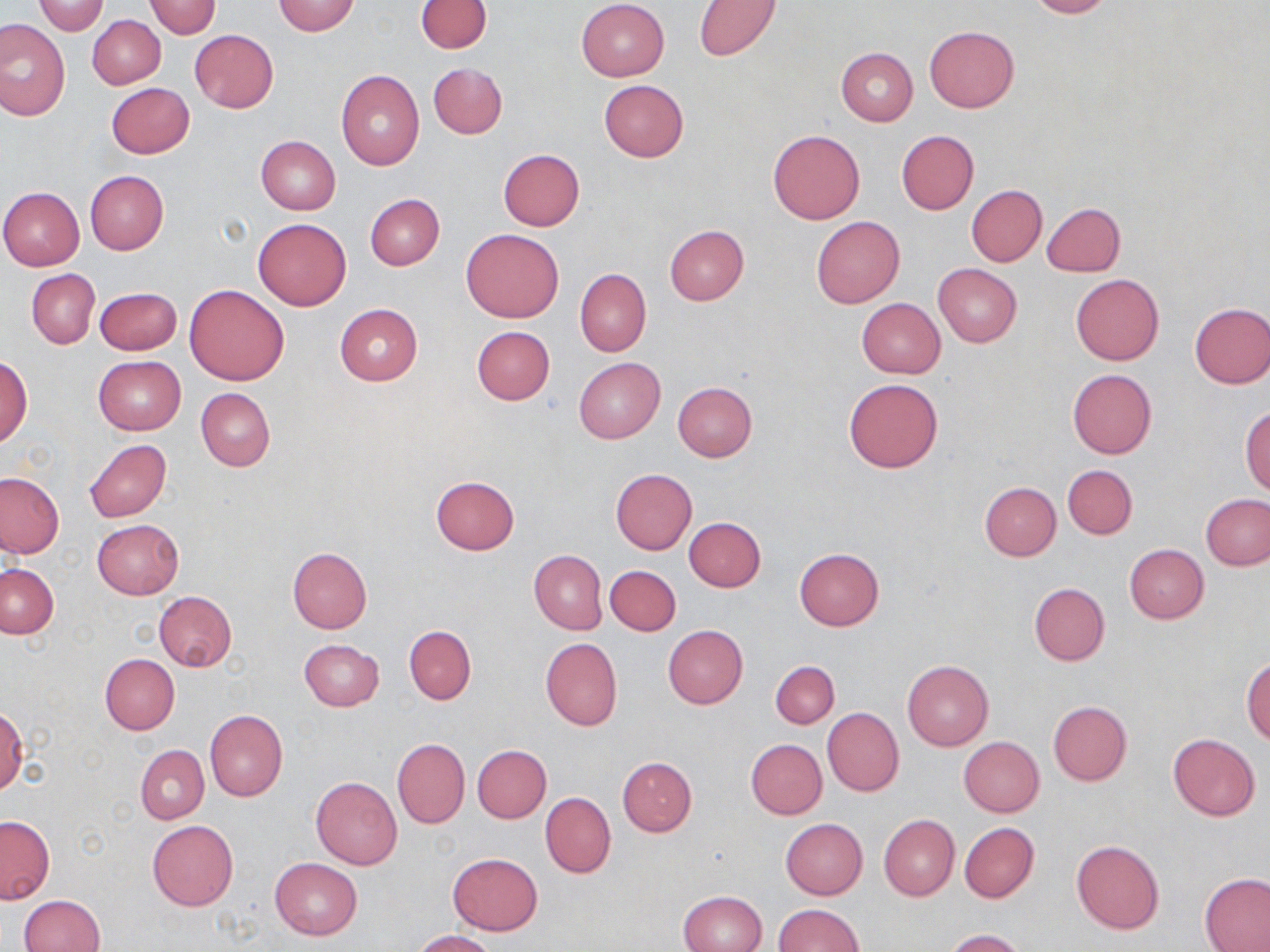
slide-level diagnosis = no evidence of blood parasites
field of view = single
preparation = thin blood film
magnification = 1000x
image size = 1270×952 pixels
uninfected red blood cell locations = approximate bounding boxes as [x1, y1, x2, y2] in pixels: [416, 0, 491, 53], [1025, 0, 1115, 18], [33, 1, 108, 36], [272, 1, 360, 36], [576, 1, 669, 81], [694, 1, 781, 61], [145, 2, 221, 38], [87, 16, 165, 89], [0, 21, 69, 119], [924, 25, 1019, 113], [190, 30, 278, 113], [837, 48, 917, 125], [428, 62, 506, 138], [336, 71, 425, 170], [598, 79, 688, 162], [106, 83, 195, 158], [768, 129, 865, 224], [896, 130, 979, 214], [256, 135, 341, 215], [498, 148, 585, 230], [84, 171, 169, 254], [966, 185, 1046, 266], [0, 186, 85, 270], [366, 193, 445, 271], [1043, 202, 1125, 277], [811, 216, 905, 309], [253, 218, 352, 310], [664, 224, 749, 305], [461, 228, 565, 323], [933, 263, 1021, 347], [575, 268, 651, 356], [27, 269, 100, 348], [1070, 274, 1163, 366], [186, 284, 289, 385], [94, 287, 182, 355], [856, 298, 945, 378], [1190, 302, 1270, 388], [335, 304, 423, 385], [471, 326, 555, 405], [93, 355, 186, 435], [0, 356, 32, 446], [574, 358, 665, 443], [1066, 369, 1157, 458], [843, 377, 943, 472], [673, 382, 758, 462], [196, 387, 275, 471], [1241, 405, 1270, 496], [84, 439, 171, 523], [1063, 465, 1138, 539], [611, 469, 697, 554], [0, 472, 65, 559], [430, 475, 519, 556], [980, 481, 1061, 561], [1201, 493, 1270, 571], [684, 516, 765, 592], [93, 519, 183, 598], [1124, 544, 1208, 624], [287, 547, 372, 633], [794, 548, 885, 630], [529, 550, 607, 635], [1, 564, 58, 638], [605, 565, 680, 635], [1028, 582, 1109, 666], [153, 590, 236, 671], [662, 625, 747, 710], [404, 626, 477, 703], [540, 638, 622, 731], [299, 639, 385, 710], [100, 654, 179, 734], [1243, 658, 1270, 745], [902, 660, 994, 749], [770, 661, 839, 728], [1048, 701, 1132, 785], [0, 704, 28, 796], [822, 708, 903, 796], [205, 710, 288, 802], [1168, 734, 1260, 821], [959, 736, 1045, 817], [392, 738, 470, 829], [746, 739, 827, 820], [135, 745, 209, 823], [473, 745, 551, 823], [617, 756, 697, 836], [311, 776, 402, 869], [540, 792, 616, 878], [878, 814, 959, 902], [0, 817, 54, 903], [780, 818, 868, 900], [147, 821, 238, 912], [959, 822, 1039, 903], [1071, 840, 1164, 934], [449, 853, 542, 934], [270, 858, 362, 940], [1200, 872, 1270, 952], [678, 890, 768, 952], [19, 894, 104, 952], [773, 904, 864, 951], [945, 929, 1028, 952], [412, 930, 496, 952]
modality = light microscopy
stain = May-Grünwald-Giemsa